State the preparation type.
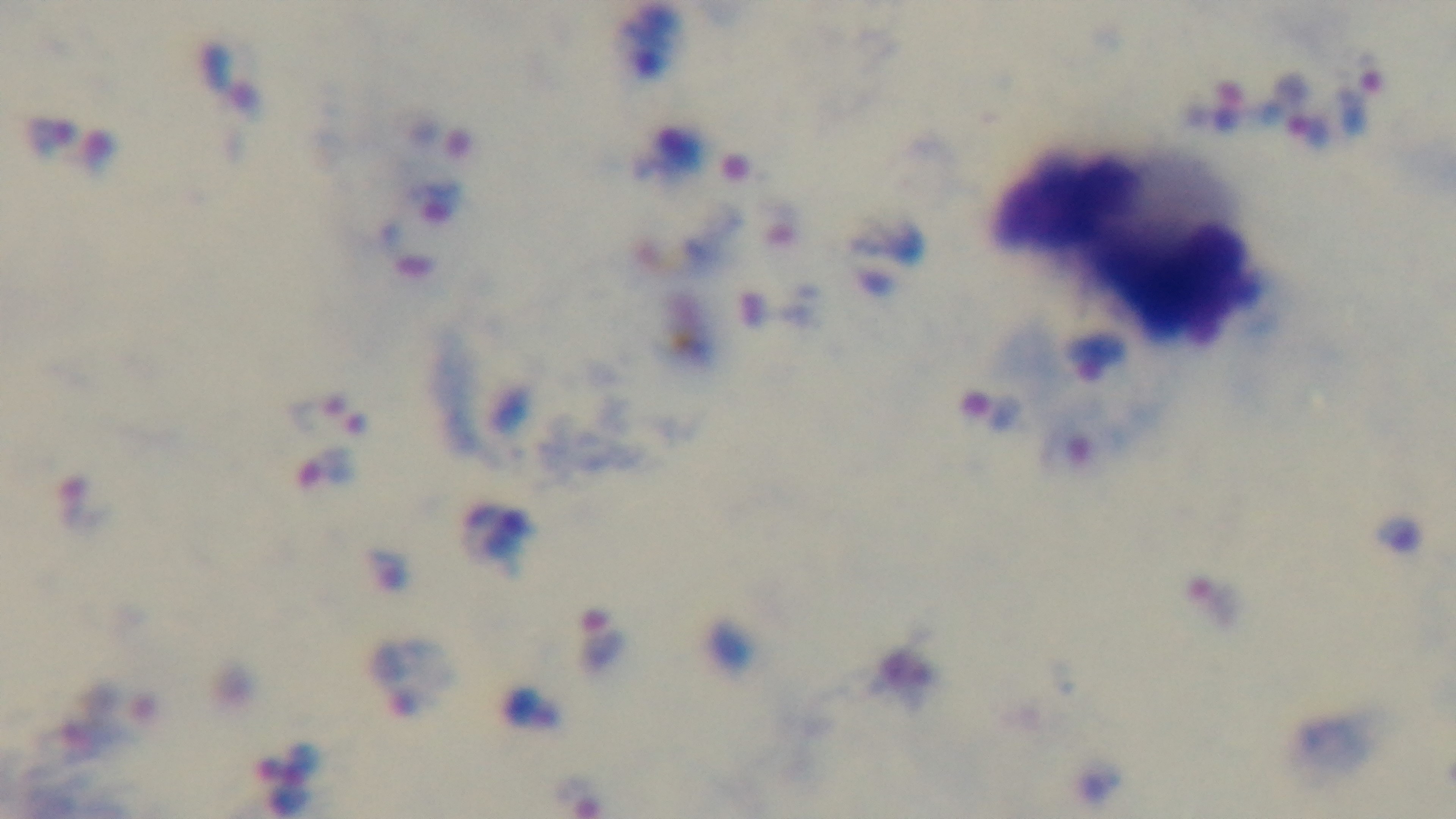

A thick smear.

capture: mounted 4K digital camera
modality: light microscopy
malaria_status: positive
objective: 100x oil immersion
stain: Giemsa
field_of_view: one from the slide